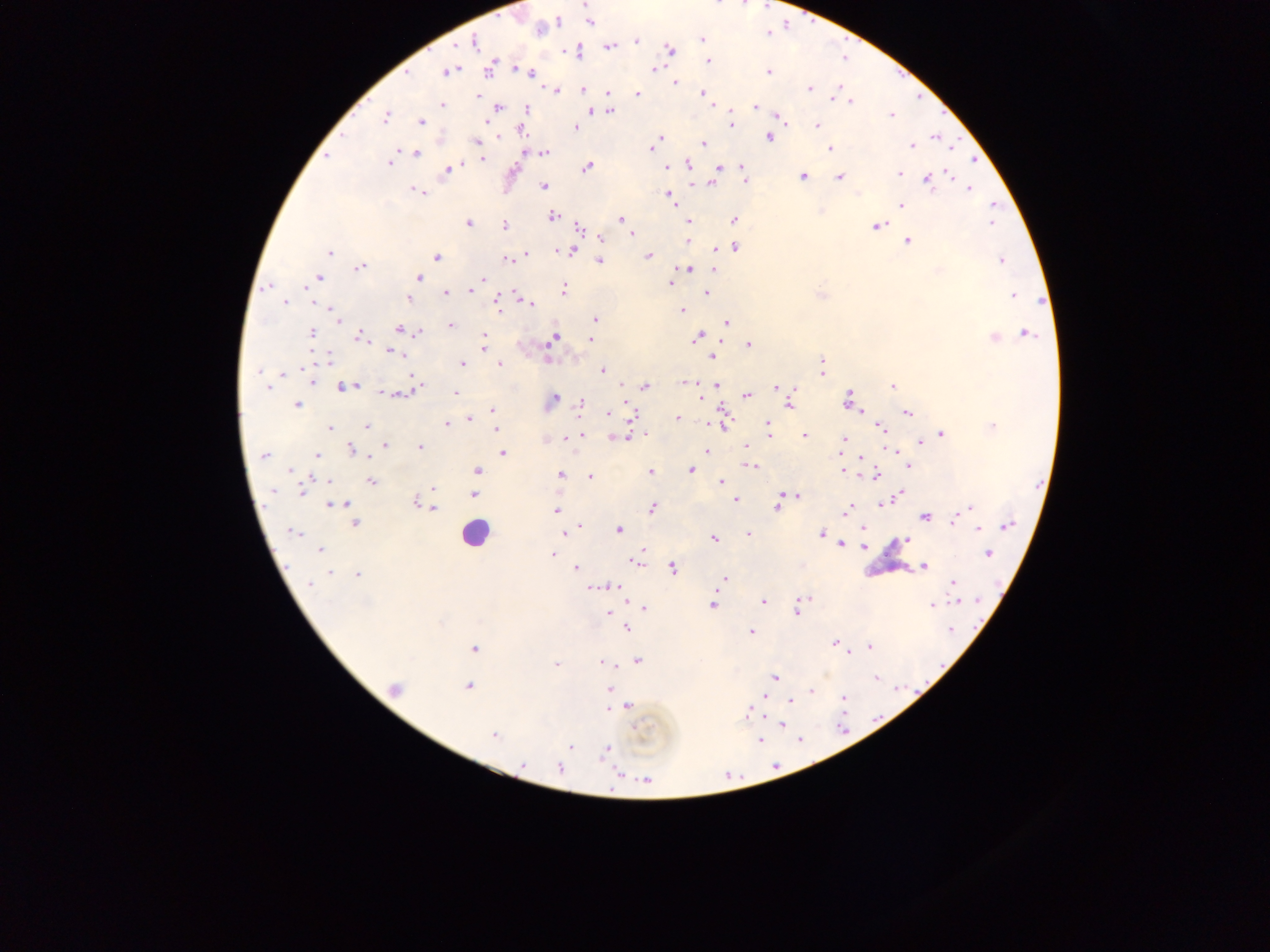 Approximate centers as (x, y) in pixels. Malaria parasite locations: (586, 4), (590, 22), (557, 23), (701, 40), (636, 41), (473, 42), (608, 47), (669, 50), (709, 61), (490, 68), (518, 68), (655, 69), (447, 72), (768, 72), (530, 73), (675, 83), (810, 89), (556, 90), (583, 90), (609, 94), (637, 94), (703, 94), (836, 94), (479, 96), (851, 101), (442, 104), (712, 105), (756, 107), (498, 108), (527, 109), (593, 110), (609, 111), (779, 116), (891, 116), (386, 117), (421, 122), (731, 124), (817, 125), (576, 128), (522, 130), (660, 137), (769, 138), (935, 138), (477, 141), (656, 142), (704, 143), (911, 145), (652, 148), (829, 149), (545, 152), (417, 153), (327, 157), (481, 160), (389, 162), (688, 165), (587, 167), (667, 168), (719, 168), (743, 168), (448, 170), (898, 173), (803, 176), (840, 177), (928, 179), (745, 181), (712, 183), (543, 186), (969, 188), (417, 192), (671, 197), (901, 205), (993, 205), (553, 216), (620, 220), (734, 220), (688, 221), (469, 223), (991, 223), (504, 225), (878, 225), (579, 228), (632, 233), (602, 239), (687, 240), (908, 241), (734, 247), (571, 251), (329, 253), (526, 255), (649, 256), (436, 257), (507, 260), (1001, 260), (600, 261), (360, 267), (688, 269), (714, 270), (938, 270), (318, 277), (419, 278), (481, 279), (670, 284), (473, 286), (267, 287), (563, 289), (471, 291), (446, 293), (707, 293), (1013, 296), (408, 299), (285, 302), (498, 304), (529, 304), (682, 310), (595, 318), (338, 319), (727, 323), (450, 325), (400, 330), (311, 333), (419, 333), (1026, 334), (360, 336), (484, 336), (697, 337), (994, 337), (554, 338), (590, 339), (749, 346), (483, 349), (392, 353), (713, 357), (327, 358), (462, 364), (500, 364), (603, 370), (259, 371), (822, 371), (284, 373), (413, 378), (310, 381), (688, 381), (717, 385), (267, 386), (892, 386), (345, 387), (645, 387), (413, 388), (776, 388), (794, 389), (456, 393), (396, 394), (747, 395), (702, 397), (848, 399), (552, 400), (580, 403), (297, 404), (789, 405), (492, 409), (609, 413), (907, 413), (633, 415), (469, 418), (677, 418), (447, 424), (767, 424), (722, 425), (366, 426), (494, 427), (880, 427), (993, 427), (329, 428), (941, 434), (582, 435), (805, 436), (567, 438), (618, 438), (844, 439), (921, 442), (385, 445), (745, 446), (420, 447), (352, 450), (890, 450), (706, 451), (503, 453), (840, 453), (264, 456), (317, 456), (861, 457), (908, 465), (751, 466), (290, 470), (477, 470), (691, 470), (843, 471), (651, 473), (560, 475), (875, 475), (590, 476), (371, 481), (721, 482), (433, 488), (303, 489), (274, 490), (786, 494), (899, 494), (473, 495), (797, 496), (735, 500), (884, 503), (417, 504), (336, 505), (425, 506), (777, 507), (970, 507), (432, 508), (652, 508), (556, 510), (847, 510), (925, 517), (954, 519), (354, 523), (1008, 525), (863, 528), (978, 529), (568, 530), (618, 530), (293, 532), (747, 534), (821, 534), (714, 538), (906, 541), (841, 544), (863, 547), (320, 549), (988, 553), (552, 554), (636, 562), (924, 566), (576, 569), (673, 569), (329, 573), (357, 575), (724, 579), (953, 583), (310, 584), (610, 586), (600, 587), (592, 588), (805, 599), (763, 601), (958, 601), (713, 605), (931, 605), (799, 606), (643, 607), (796, 612), (608, 613), (627, 628), (951, 629), (751, 632), (835, 644), (869, 646), (474, 649), (846, 652), (638, 660), (602, 663), (556, 665), (775, 677), (876, 677), (468, 686), (395, 688), (608, 690), (811, 691), (844, 698), (790, 701), (628, 706), (749, 712), (781, 725), (637, 729), (494, 735), (800, 739), (761, 740), (570, 747), (606, 750), (523, 765), (776, 766), (559, 768), (646, 780). Leukocyte locations: (473, 534). Single field of view. Image is 1270×952 pixels. Sample from Ghana. Thick blood film. Photographed through a microscope with a mobile-phone camera.